State the blood parasite species.
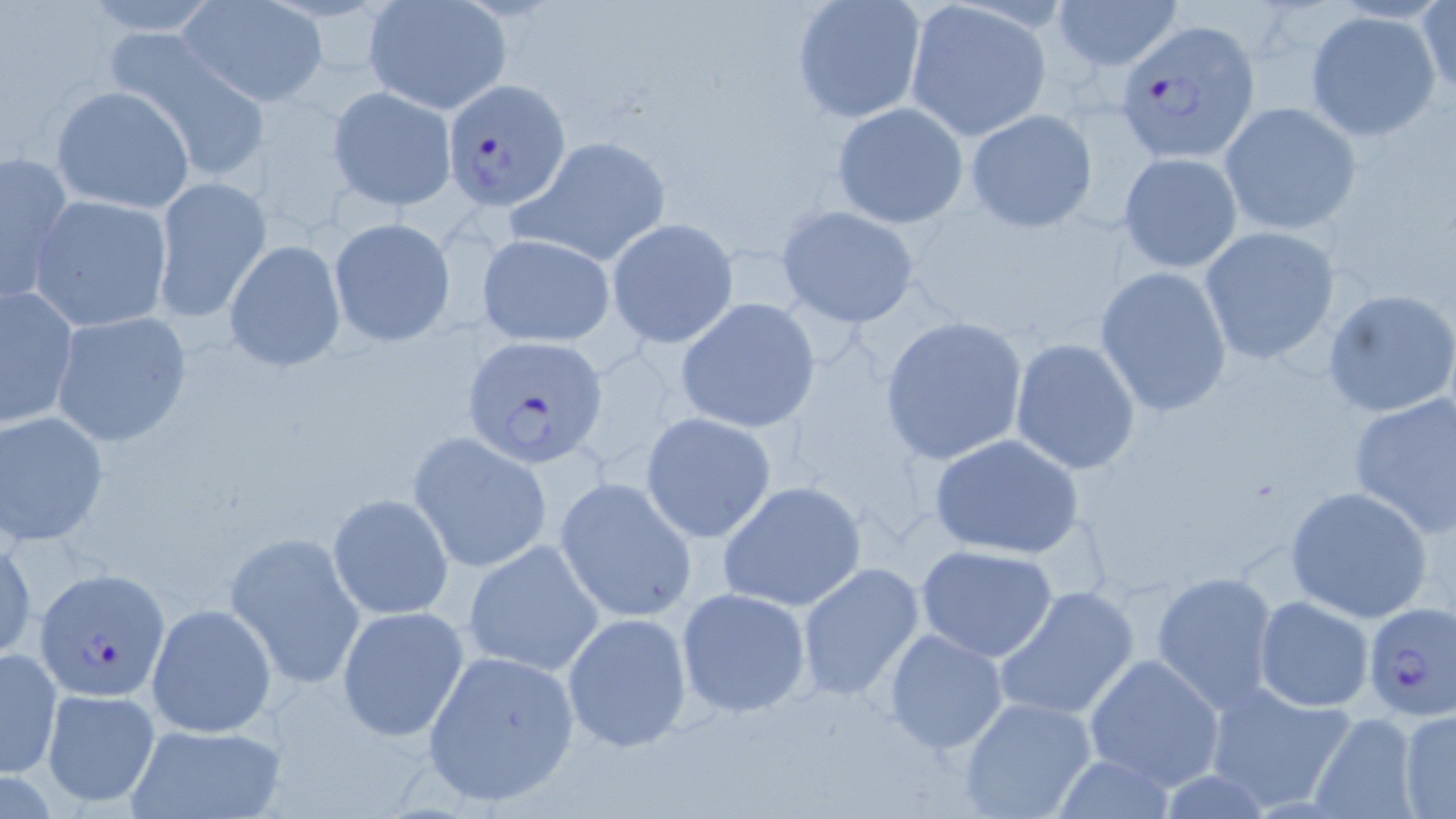

Plasmodium falciparum.

image size = 1456×819 pixels
modality = optical microscopy
preparation = thin blood smear
field of view = single
magnification = 1000x
stain = May-Grünwald-Giemsa
Plasmodium falciparum-infected red blood cell locations = approximate bounding boxes as (x1, y1, x2, y2) in pixels: (1115, 20, 1261, 162), (442, 79, 571, 213), (463, 335, 608, 468), (34, 568, 168, 701), (1361, 602, 1456, 725)
uninfected red blood cell locations = approximate bounding boxes as (x1, y1, x2, y2) in pixels: (1054, 0, 1183, 73), (362, 1, 513, 115), (791, 1, 927, 123), (903, 1, 1052, 141), (1417, 1, 1455, 101), (178, 2, 326, 107), (1305, 10, 1441, 142), (112, 33, 274, 184), (50, 86, 196, 213), (326, 86, 457, 210), (831, 102, 968, 229), (1219, 102, 1360, 235), (965, 106, 1100, 232), (518, 135, 672, 266), (2, 149, 76, 307), (1118, 152, 1244, 272), (152, 178, 273, 326), (27, 195, 175, 333), (775, 204, 921, 328), (328, 217, 456, 347), (606, 219, 739, 348), (1197, 226, 1344, 366), (477, 232, 616, 347), (223, 239, 346, 373), (1094, 267, 1234, 418), (1, 284, 79, 428), (1321, 286, 1456, 419), (676, 298, 822, 434), (50, 311, 194, 447), (878, 315, 1028, 466), (1010, 338, 1142, 475), (1347, 391, 1456, 537), (1, 410, 109, 546), (640, 412, 777, 542), (409, 433, 552, 573), (928, 434, 1084, 561), (555, 478, 698, 623), (718, 480, 868, 613), (1284, 486, 1435, 623), (327, 492, 453, 620), (226, 531, 365, 690), (1, 533, 36, 663), (461, 540, 605, 677), (915, 544, 1062, 662), (796, 562, 925, 702), (1152, 571, 1279, 710), (993, 585, 1140, 722), (676, 588, 813, 718), (1254, 596, 1373, 712), (145, 603, 277, 740), (336, 605, 470, 740), (561, 612, 692, 751), (882, 628, 1010, 756), (2, 646, 62, 778), (422, 648, 581, 809), (1083, 653, 1225, 790), (1202, 679, 1359, 814), (41, 688, 161, 809), (956, 695, 1099, 819), (1397, 709, 1456, 817), (1306, 713, 1417, 819), (123, 722, 287, 819)